Identify the blood parasite species.
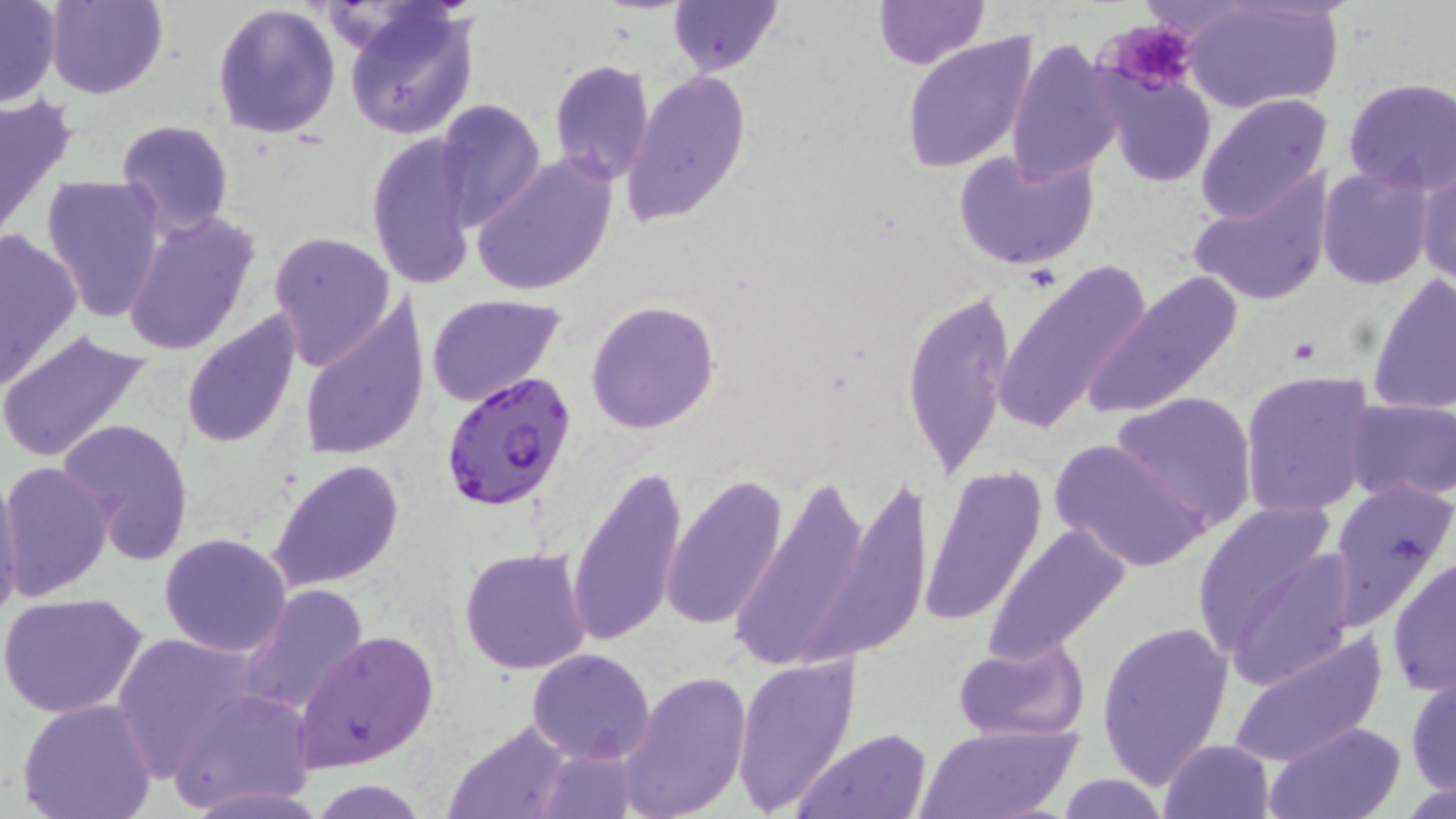

Plasmodium falciparum.

magnification: 1000x
plasmodium_falciparum_infected_red_blood_cell_locations: 'approximate bounding boxes as named x1/y1/x2/y2 corners in pixels: (x1=441, y1=368, x2=576, y2=511)'
stain: May-Grünwald-Giemsa
uninfected_red_blood_cell_locations: 'approximate bounding boxes as named x1/y1/x2/y2 corners in pixels: (x1=45, y1=0, x2=166, y2=100), (x1=668, y1=0, x2=781, y2=75), (x1=873, y1=0, x2=987, y2=70), (x1=1179, y1=1, x2=1344, y2=113), (x1=0, y1=2, x2=61, y2=108), (x1=213, y1=2, x2=342, y2=140), (x1=342, y1=3, x2=479, y2=140), (x1=900, y1=32, x2=1040, y2=176), (x1=1006, y1=35, x2=1122, y2=184), (x1=549, y1=59, x2=654, y2=184), (x1=620, y1=68, x2=751, y2=227), (x1=1100, y1=68, x2=1215, y2=189), (x1=1343, y1=76, x2=1456, y2=196), (x1=0, y1=90, x2=78, y2=246), (x1=1196, y1=93, x2=1333, y2=223), (x1=433, y1=100, x2=548, y2=231), (x1=116, y1=119, x2=234, y2=238), (x1=365, y1=132, x2=481, y2=291), (x1=953, y1=146, x2=1099, y2=269), (x1=471, y1=154, x2=618, y2=298), (x1=1416, y1=164, x2=1456, y2=288), (x1=1317, y1=165, x2=1435, y2=291), (x1=1186, y1=167, x2=1335, y2=308), (x1=41, y1=174, x2=165, y2=323), (x1=122, y1=210, x2=263, y2=360), (x1=0, y1=224, x2=85, y2=392), (x1=266, y1=231, x2=396, y2=368), (x1=993, y1=260, x2=1151, y2=437), (x1=1082, y1=270, x2=1246, y2=419), (x1=1368, y1=274, x2=1456, y2=417), (x1=903, y1=287, x2=1013, y2=481), (x1=425, y1=294, x2=566, y2=407), (x1=297, y1=298, x2=430, y2=461), (x1=586, y1=300, x2=720, y2=434), (x1=179, y1=311, x2=304, y2=451), (x1=0, y1=325, x2=154, y2=463), (x1=1239, y1=370, x2=1377, y2=519), (x1=1109, y1=390, x2=1257, y2=528), (x1=1344, y1=396, x2=1456, y2=503), (x1=58, y1=416, x2=196, y2=562), (x1=1049, y1=438, x2=1212, y2=572), (x1=268, y1=458, x2=405, y2=592), (x1=0, y1=460, x2=116, y2=602), (x1=566, y1=464, x2=688, y2=651), (x1=723, y1=465, x2=880, y2=675), (x1=919, y1=465, x2=1049, y2=627), (x1=0, y1=468, x2=25, y2=625), (x1=661, y1=474, x2=787, y2=629), (x1=1327, y1=479, x2=1456, y2=628), (x1=1193, y1=506, x2=1353, y2=683), (x1=983, y1=525, x2=1129, y2=662), (x1=158, y1=533, x2=293, y2=659), (x1=459, y1=547, x2=592, y2=675), (x1=1386, y1=554, x2=1456, y2=697), (x1=236, y1=582, x2=368, y2=720), (x1=1, y1=591, x2=150, y2=720), (x1=1096, y1=620, x2=1235, y2=790), (x1=112, y1=630, x2=259, y2=776), (x1=292, y1=630, x2=439, y2=769), (x1=1224, y1=631, x2=1388, y2=770), (x1=953, y1=639, x2=1088, y2=743), (x1=526, y1=647, x2=657, y2=765), (x1=734, y1=655, x2=858, y2=811), (x1=618, y1=669, x2=753, y2=819), (x1=1405, y1=673, x2=1455, y2=798), (x1=168, y1=689, x2=318, y2=813), (x1=15, y1=698, x2=159, y2=819), (x1=442, y1=720, x2=574, y2=819), (x1=1267, y1=720, x2=1405, y2=817), (x1=915, y1=725, x2=1080, y2=819), (x1=793, y1=727, x2=932, y2=818), (x1=1157, y1=738, x2=1276, y2=819), (x1=535, y1=742, x2=636, y2=818), (x1=1055, y1=774, x2=1172, y2=817), (x1=311, y1=781, x2=428, y2=818)'
image_size: 1456×819 pixels
field_of_view: one of a larger specimen
modality: light microscopy
preparation: thin blood smear
platelet_locations: 'approximate bounding boxes as named x1/y1/x2/y2 corners in pixels: (x1=1103, y1=18, x2=1198, y2=94)'